Identify the parasite.
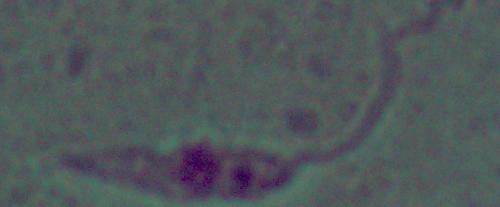
Leishmania.

Photomicrograph. 1000x magnification.